Classify this cell by malaria status.
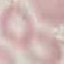

It is uninfected.

{
  "stain": "Giemsa",
  "capture": "smartphone camera at the microscope eyepiece",
  "preparation": "thin blood film",
  "image_type": "cell patch, automatically extracted from a larger field of view and resized to 64 × 64 pixels"
}